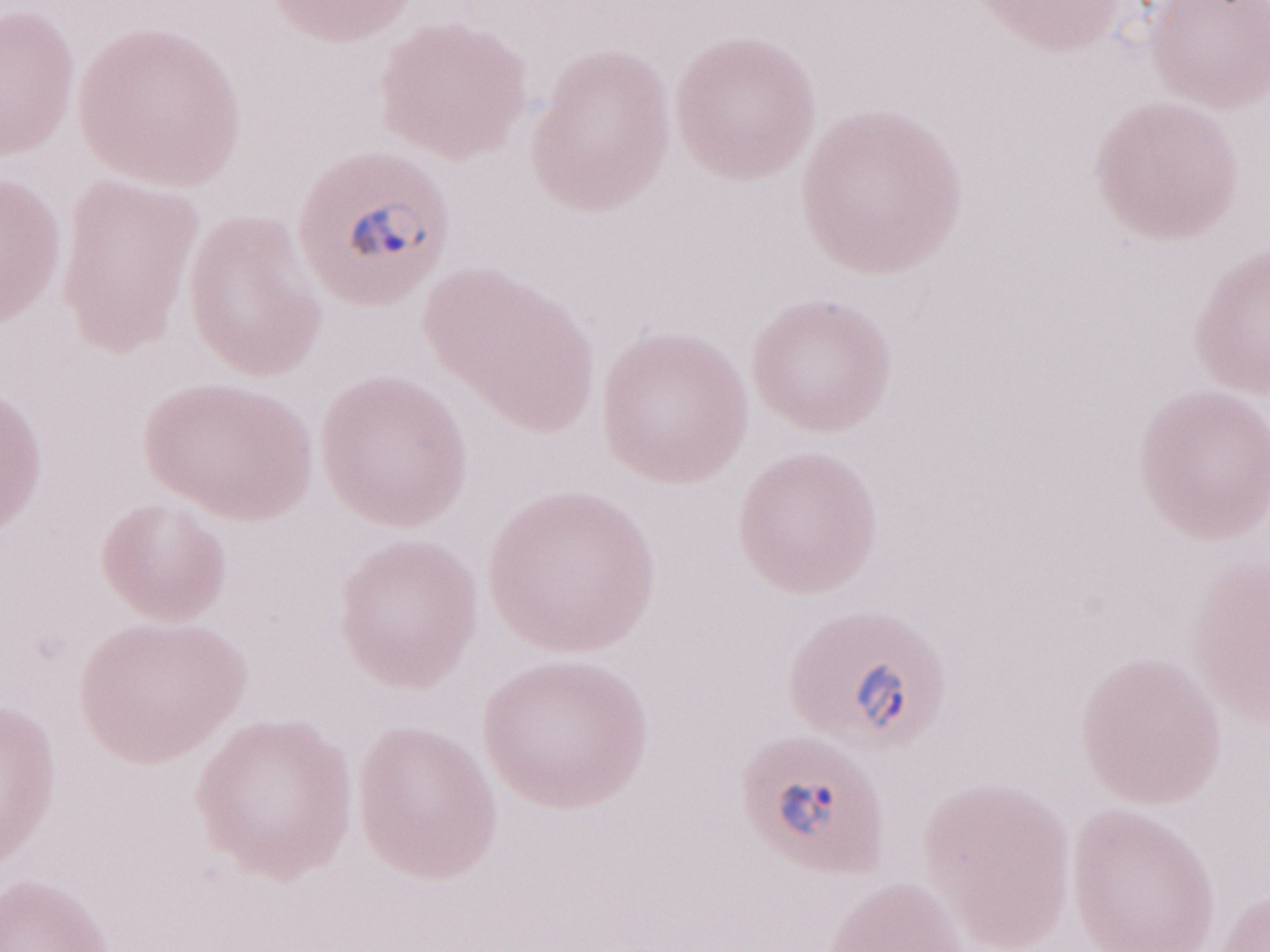

Olympus BX43 microscope and DP73 digital camera. Single field of view. Thin peripheral-blood smear. May-Grünwald-Giemsa (MGG) stain. Image is 1270×952 pixels. 1,000x magnification. Malaria diagnosis (patient-level): positive.